Identify the preparation type.
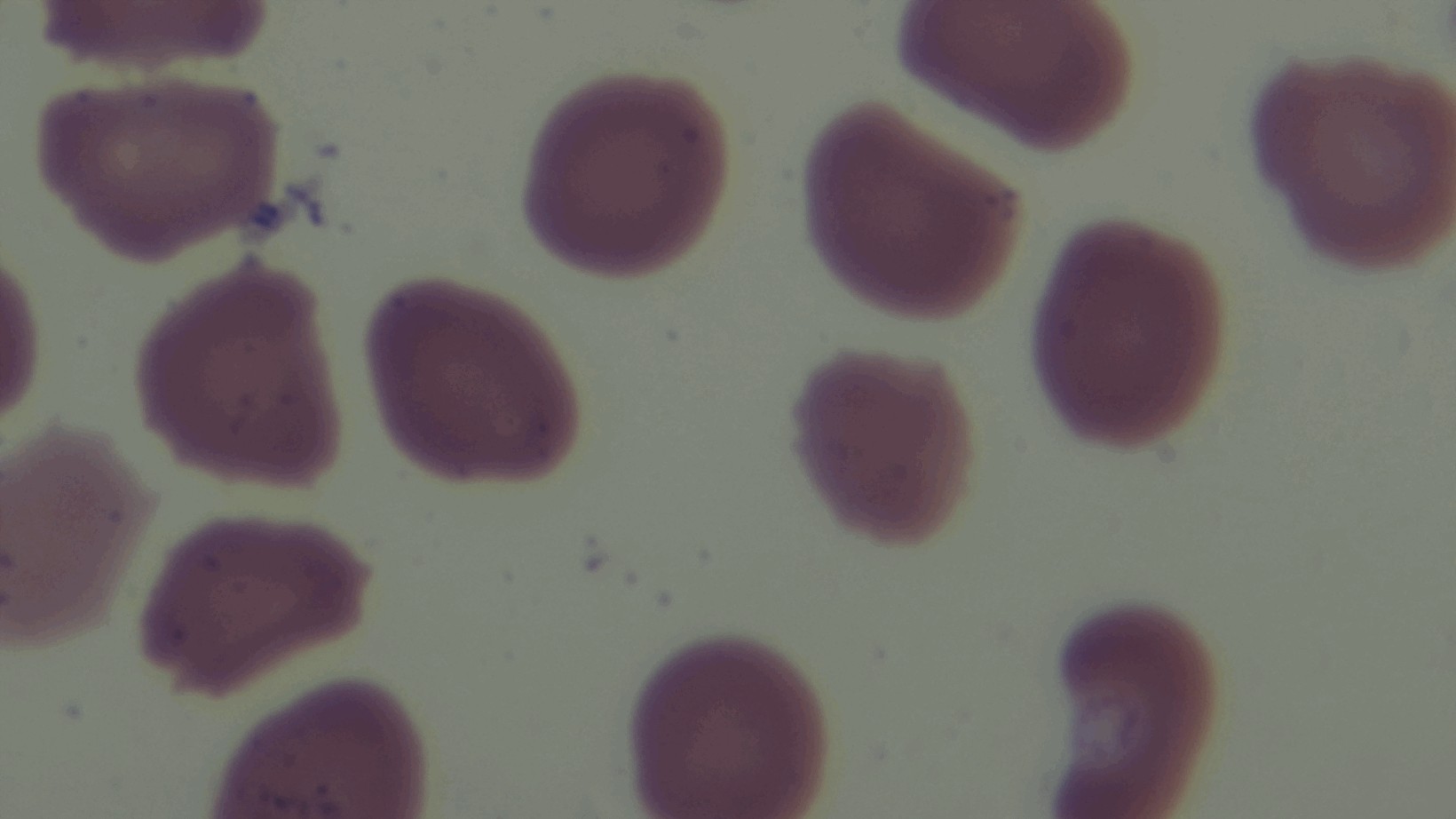

A thin smear.

Malaria status: uninfected. Captured with a mounted 4K digital camera. 100x oil-immersion objective. Photomicrograph. Giemsa stain. One field from the slide.